Give the extent of all Plasmodium ovale-infected red blood cells.
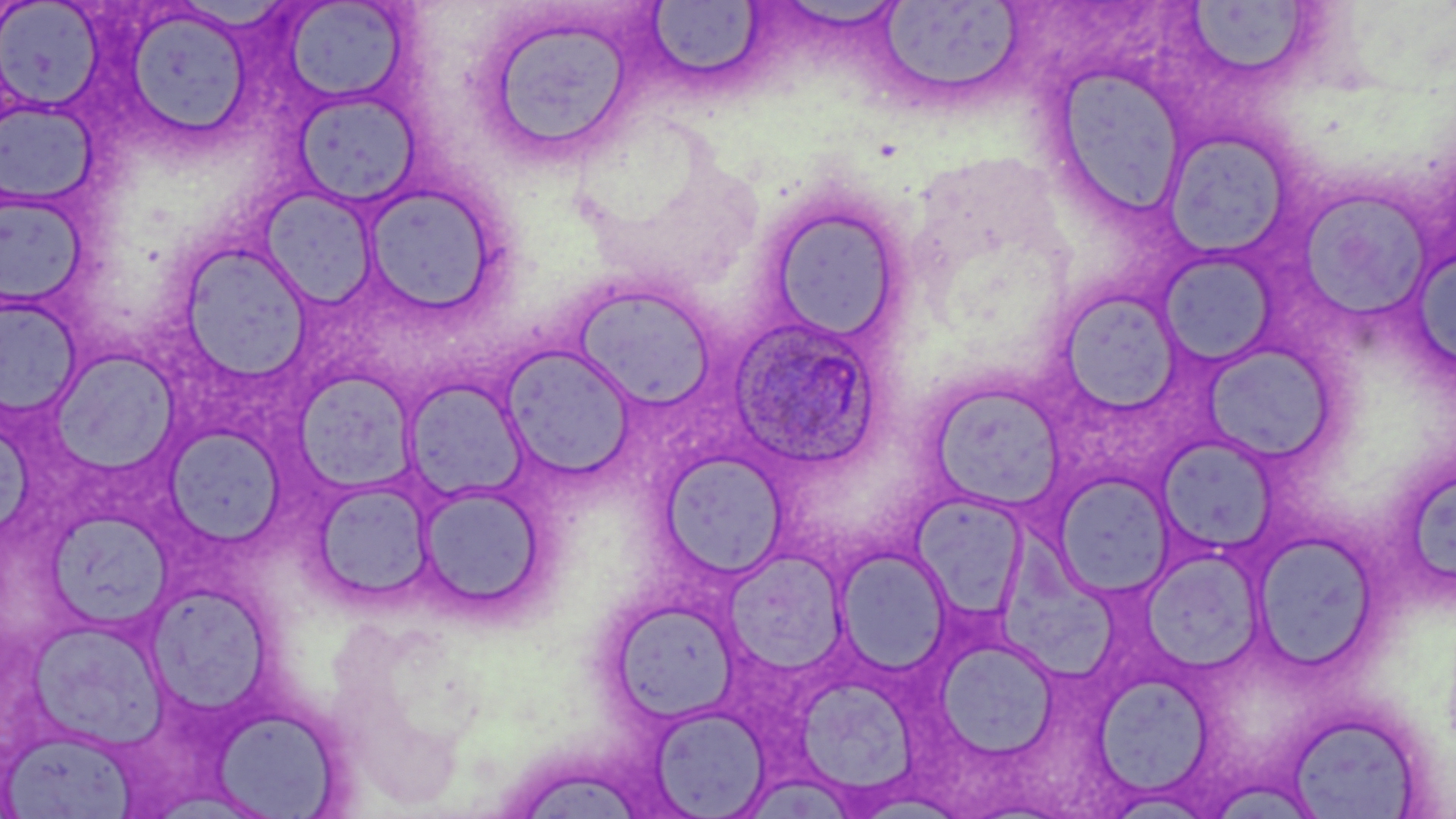

Approximate bounding boxes as named x1/y1/x2/y2 corners in pixels.
Plasmodium ovale-infected red blood cells: (x1=728, y1=316, x2=882, y2=469).

Summary:
  - Uninfected red blood cell locations: (x1=0, y1=1, x2=103, y2=111), (x1=283, y1=1, x2=409, y2=103), (x1=877, y1=1, x2=1025, y2=101), (x1=1184, y1=2, x2=1317, y2=77), (x1=646, y1=3, x2=765, y2=80), (x1=123, y1=9, x2=252, y2=142), (x1=480, y1=10, x2=649, y2=167), (x1=1051, y1=64, x2=1188, y2=221), (x1=292, y1=91, x2=422, y2=208), (x1=0, y1=101, x2=96, y2=205), (x1=1161, y1=130, x2=1295, y2=260), (x1=362, y1=183, x2=500, y2=315), (x1=257, y1=188, x2=379, y2=310), (x1=1297, y1=188, x2=1435, y2=322), (x1=0, y1=191, x2=89, y2=309), (x1=763, y1=201, x2=906, y2=344), (x1=177, y1=242, x2=313, y2=380), (x1=1409, y1=243, x2=1456, y2=368), (x1=1157, y1=252, x2=1277, y2=365), (x1=571, y1=282, x2=717, y2=411), (x1=1057, y1=290, x2=1183, y2=413), (x1=0, y1=297, x2=81, y2=417), (x1=498, y1=344, x2=637, y2=480), (x1=1201, y1=345, x2=1334, y2=464), (x1=55, y1=347, x2=188, y2=471), (x1=295, y1=372, x2=419, y2=495), (x1=403, y1=379, x2=528, y2=503), (x1=927, y1=381, x2=1066, y2=510), (x1=167, y1=429, x2=283, y2=544), (x1=1157, y1=436, x2=1278, y2=556), (x1=661, y1=452, x2=786, y2=578), (x1=1054, y1=474, x2=1172, y2=596), (x1=1408, y1=474, x2=1456, y2=589), (x1=313, y1=480, x2=435, y2=604), (x1=418, y1=484, x2=548, y2=616), (x1=911, y1=493, x2=1029, y2=621), (x1=49, y1=511, x2=171, y2=630), (x1=996, y1=519, x2=1118, y2=687), (x1=1253, y1=533, x2=1378, y2=667), (x1=835, y1=547, x2=952, y2=675), (x1=729, y1=548, x2=846, y2=683), (x1=1145, y1=549, x2=1262, y2=672), (x1=147, y1=581, x2=268, y2=717), (x1=610, y1=600, x2=739, y2=722), (x1=28, y1=619, x2=166, y2=749), (x1=937, y1=637, x2=1058, y2=759), (x1=1094, y1=672, x2=1214, y2=795), (x1=795, y1=675, x2=918, y2=797), (x1=649, y1=706, x2=770, y2=816), (x1=213, y1=707, x2=342, y2=818), (x1=1287, y1=711, x2=1425, y2=818), (x1=4, y1=730, x2=135, y2=817), (x1=525, y1=770, x2=646, y2=819), (x1=751, y1=776, x2=862, y2=819)
  - Slide-level diagnosis: Plasmodium ovale
  - Field of view: single
  - Preparation: thin blood film
  - Modality: optical microscopy
  - Magnification: 1000x
  - Stain: May-Grünwald-Giemsa
  - Image size: 1456×819 pixels